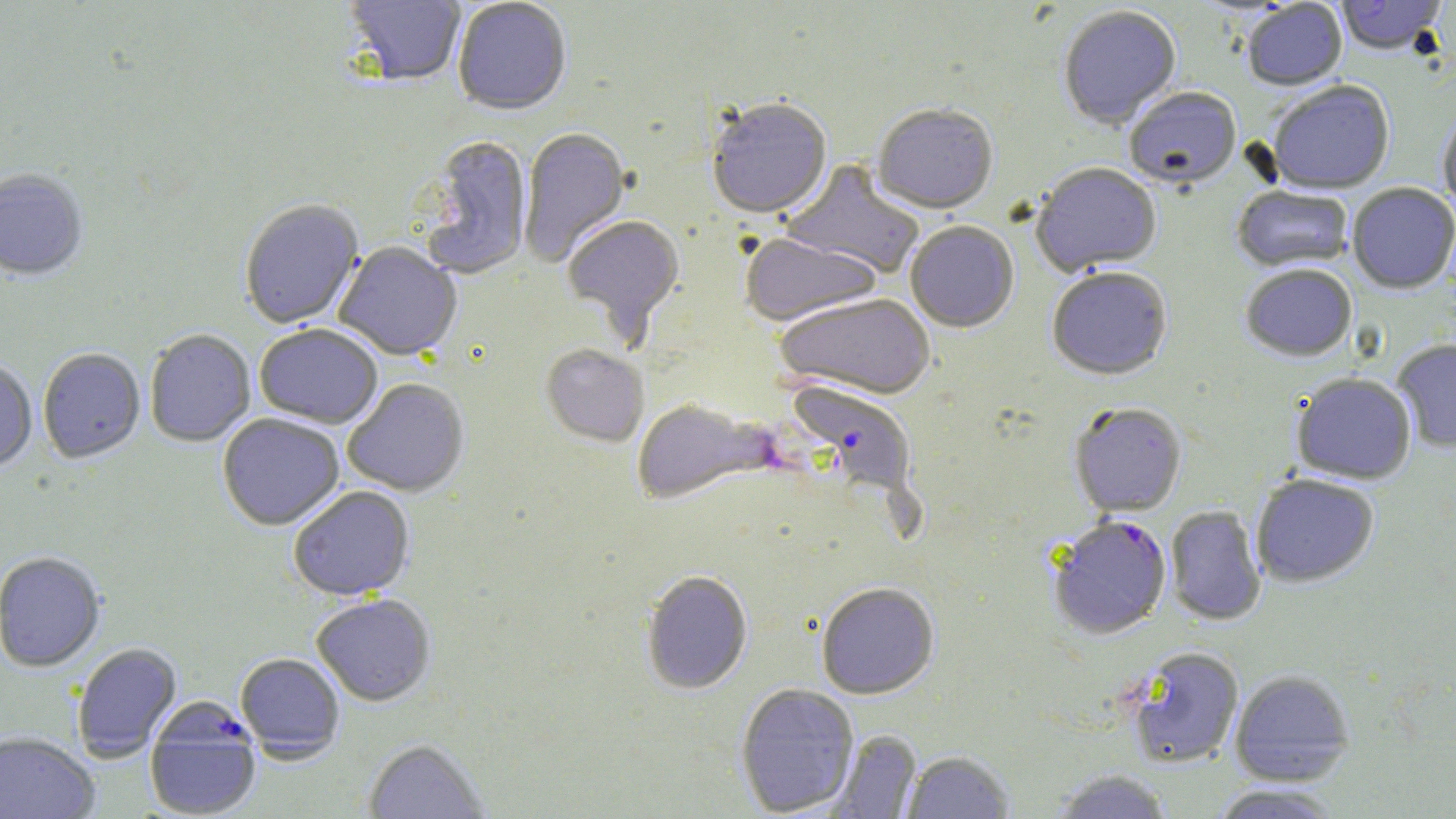

Summary:
  - Coordinate format: approximate bounding boxes as (x1, y1, x2, y2) in pixels
  - Uninfected red blood cell locations: (452, 0, 572, 117), (1334, 0, 1449, 57), (342, 1, 466, 89), (1241, 2, 1347, 93), (1058, 7, 1182, 131), (1269, 82, 1395, 196), (1124, 89, 1242, 192), (707, 100, 832, 222), (872, 106, 998, 216), (1438, 109, 1456, 219), (518, 128, 631, 268), (419, 137, 532, 281), (781, 159, 925, 280), (1031, 164, 1162, 277), (0, 169, 89, 282), (1347, 184, 1456, 295), (1232, 187, 1353, 274), (239, 200, 364, 330), (561, 215, 685, 344), (905, 222, 1019, 334), (741, 234, 881, 328), (334, 243, 462, 361), (1241, 266, 1357, 363), (1046, 269, 1173, 381), (774, 294, 937, 400), (254, 324, 383, 429), (145, 329, 256, 448), (1392, 340, 1456, 453), (540, 345, 649, 448), (37, 348, 146, 465), (0, 360, 37, 475), (1292, 374, 1417, 485), (342, 379, 470, 497), (632, 399, 776, 507), (1069, 403, 1187, 517), (217, 413, 345, 530), (1251, 474, 1379, 588), (287, 486, 415, 600), (1164, 505, 1266, 626), (0, 552, 106, 673), (640, 571, 753, 694), (816, 582, 939, 700), (311, 595, 436, 707), (71, 643, 182, 761), (1125, 647, 1244, 768), (235, 653, 345, 761), (1229, 670, 1355, 786), (735, 683, 860, 817), (828, 730, 922, 818), (0, 732, 100, 819), (362, 739, 491, 818), (901, 750, 1015, 818), (1050, 769, 1175, 818), (1208, 783, 1344, 819)
  - Plasmodium falciparum-infected red blood cell locations: (784, 382, 919, 500), (1047, 515, 1172, 640), (145, 701, 262, 819)
  - Slide-level diagnosis: Plasmodium falciparum
  - Preparation: thin blood film
  - Stain: May-Grünwald-Giemsa
  - Magnification: 1000x
  - Image size: 1456×819 pixels
  - Field of view: one of a larger specimen
  - Modality: light microscopy